Point out each malaria parasite.
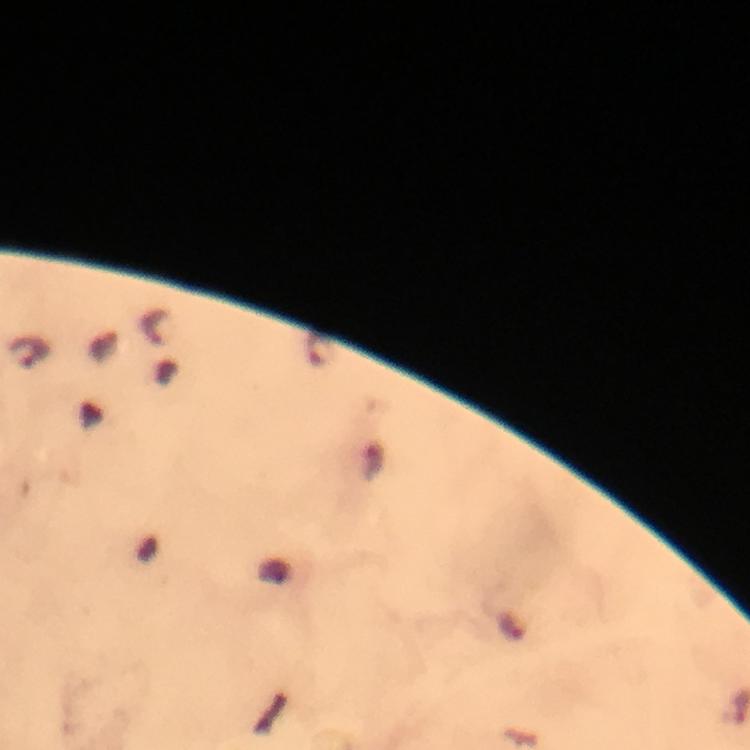

Approximate centers as [x, y] in pixels.
Malaria parasites: [156, 324], [29, 352].

Summary:
  - Magnification: 100x
  - Cropped from: one field of view
  - Preparation: thick smear
  - Capture: smartphone photograph through a microscope
  - Context: from a malaria diagnostic workup
  - Stain: Giemsa
  - Immersion oil: applied
  - Image size: 750×750 pixels